Assess this cell for malaria.
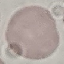
It is uninfected.

image_type: cell patch, automatically extracted from a larger field of view and resized to 64 × 64 pixels
capture: smartphone camera at the microscope eyepiece
preparation: thin blood smear
stain: Giemsa